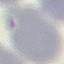

result = no malaria parasites detected
capture = smartphone camera at the microscope eyepiece
image type = cell patch, automatically extracted from a larger field of view and resized to 64 × 64 pixels
preparation = thin smear
stain = Giemsa